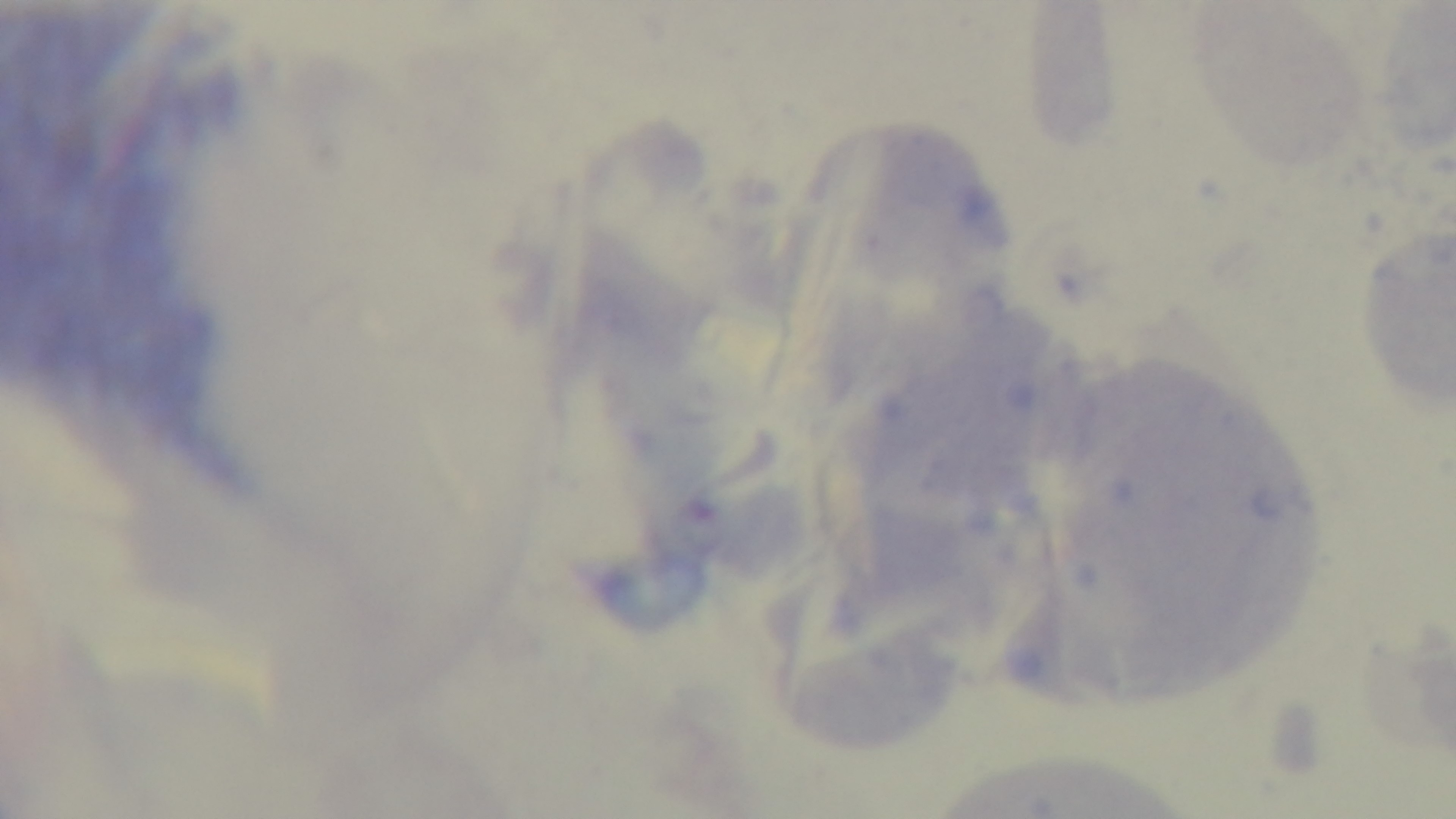 Oil-immersion objective, 100x. Light microscopy. Giemsa stain. Malaria status: negative. Preparation: thick blood film. Captured with a mounted 4K digital camera. Single field of view.